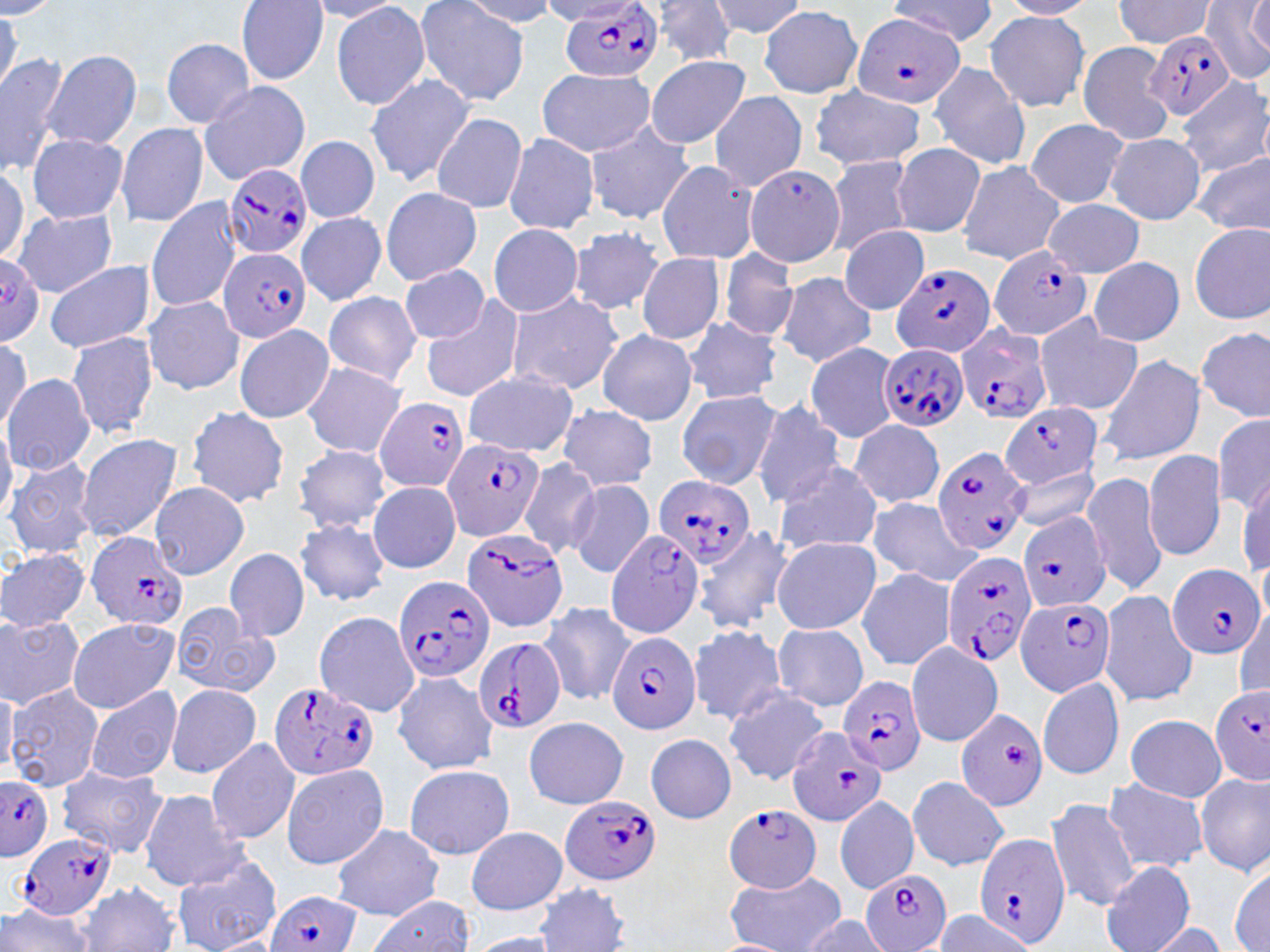
slide-level diagnosis = Plasmodium falciparum
modality = optical microscopy
image size = 1270×952 pixels
field of view = one of a larger specimen
Plasmodium falciparum-infected red blood cell locations = approximate bounding boxes as [x1, y1, x2, y2] in pixels: [562, 2, 662, 84], [852, 13, 966, 109], [1144, 29, 1236, 120], [224, 164, 312, 262], [990, 244, 1094, 341], [219, 247, 311, 343], [0, 255, 45, 342], [890, 260, 994, 360], [957, 325, 1051, 426], [876, 343, 968, 433], [374, 398, 469, 491], [1000, 402, 1102, 491], [441, 436, 546, 542], [932, 445, 1030, 555], [654, 476, 756, 564], [1018, 510, 1113, 613], [461, 526, 572, 632], [605, 528, 706, 637], [85, 530, 189, 631], [941, 551, 1040, 669], [1168, 562, 1264, 660], [390, 573, 494, 684], [1015, 595, 1118, 696], [606, 631, 701, 736], [473, 636, 565, 736], [837, 673, 928, 776], [268, 682, 380, 779], [1209, 688, 1270, 784], [954, 707, 1048, 812], [786, 727, 888, 826], [1, 776, 53, 860], [562, 794, 661, 884], [725, 804, 822, 893], [19, 830, 119, 921], [975, 834, 1072, 949], [860, 869, 951, 952], [263, 890, 359, 952]
preparation = thin blood film
stain = May-Grünwald-Giemsa
magnification = 1000x
uninfected red blood cell locations = approximate bounding boxes as [x1, y1, x2, y2] in pixels: [415, 0, 529, 110], [649, 0, 741, 65], [710, 0, 806, 39], [891, 0, 997, 47], [1115, 0, 1214, 47], [1202, 0, 1269, 81], [0, 1, 60, 19], [236, 1, 329, 84], [305, 1, 409, 22], [458, 1, 558, 25], [997, 1, 1097, 18], [1248, 1, 1268, 60], [330, 2, 430, 111], [759, 6, 862, 96], [0, 8, 22, 103], [984, 11, 1090, 113], [161, 38, 254, 127], [1077, 42, 1175, 145], [0, 50, 69, 176], [44, 50, 142, 151], [642, 55, 753, 149], [928, 60, 1030, 171], [536, 68, 657, 157], [363, 73, 477, 188], [1178, 79, 1269, 177], [197, 81, 310, 184], [808, 85, 927, 172], [708, 90, 807, 191], [431, 113, 528, 215], [1025, 119, 1131, 208], [115, 121, 210, 229], [585, 121, 695, 223], [1104, 132, 1206, 224], [26, 133, 127, 223], [502, 133, 601, 235], [295, 135, 379, 223], [892, 144, 985, 237], [1194, 151, 1270, 236], [823, 156, 918, 255], [656, 160, 760, 265], [955, 160, 1063, 265], [0, 166, 28, 262], [744, 166, 847, 267], [381, 186, 483, 285], [146, 198, 245, 313], [1043, 199, 1144, 276], [10, 207, 118, 297], [296, 213, 388, 306], [1188, 222, 1270, 324], [488, 224, 583, 317], [568, 226, 666, 316], [839, 226, 928, 314], [719, 249, 798, 342], [637, 252, 724, 345], [1088, 256, 1184, 345], [44, 260, 154, 354], [401, 265, 488, 344], [775, 272, 878, 366], [322, 290, 422, 385], [505, 290, 625, 396], [142, 295, 244, 394], [421, 295, 526, 403], [1034, 312, 1143, 417], [682, 315, 781, 405], [234, 323, 333, 423], [1198, 325, 1269, 421], [595, 329, 698, 424], [66, 331, 159, 440], [0, 335, 32, 435], [804, 342, 900, 442], [1095, 355, 1205, 466], [301, 362, 409, 458], [463, 371, 578, 456], [1, 373, 95, 476], [675, 389, 780, 489], [751, 400, 847, 509], [556, 404, 659, 491], [186, 405, 290, 508], [1212, 413, 1270, 517], [849, 418, 945, 509], [0, 419, 17, 522], [74, 431, 185, 542], [294, 445, 391, 530], [1143, 449, 1228, 562], [5, 457, 98, 559], [517, 458, 601, 560], [772, 460, 885, 558], [1009, 465, 1102, 531], [1237, 470, 1269, 579], [1082, 472, 1169, 597], [566, 479, 655, 577], [369, 480, 460, 574], [149, 481, 251, 579], [868, 499, 984, 586], [294, 518, 390, 605], [692, 526, 795, 635], [771, 536, 881, 635], [0, 547, 90, 633], [223, 548, 310, 642], [856, 568, 956, 671], [1099, 589, 1200, 706], [539, 602, 636, 706], [168, 603, 280, 698], [1234, 607, 1269, 699], [313, 612, 420, 716], [0, 616, 85, 710], [65, 617, 180, 714], [687, 624, 790, 724], [771, 625, 869, 711], [905, 641, 1004, 747], [391, 672, 497, 775], [1037, 675, 1126, 781], [0, 684, 18, 772], [7, 684, 102, 792], [722, 684, 832, 786], [165, 685, 262, 777], [86, 686, 183, 784], [1124, 712, 1226, 801], [523, 716, 629, 809], [645, 733, 736, 823], [204, 736, 301, 844], [201, 749, 382, 856], [281, 762, 389, 870], [56, 764, 167, 858], [404, 764, 514, 860], [1196, 773, 1269, 873], [906, 777, 1011, 871], [1103, 779, 1209, 872], [138, 789, 248, 890], [834, 795, 920, 895], [1045, 797, 1142, 912], [330, 824, 445, 921], [465, 827, 568, 915], [171, 850, 282, 952], [1100, 860, 1194, 952], [1230, 865, 1270, 951], [722, 866, 849, 952], [76, 881, 181, 952], [534, 883, 634, 951], [364, 896, 475, 951], [0, 901, 96, 952], [934, 910, 1038, 951], [792, 914, 891, 950], [1143, 922, 1229, 952], [463, 933, 566, 952]